Classify this cell by malaria status.
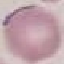
It is uninfected.

Photographed with a smartphone camera at the microscope eyepiece. Thin blood film. Cell patch, automatically extracted from a larger field of view and resized to 64 × 64 pixels. Giemsa stain.